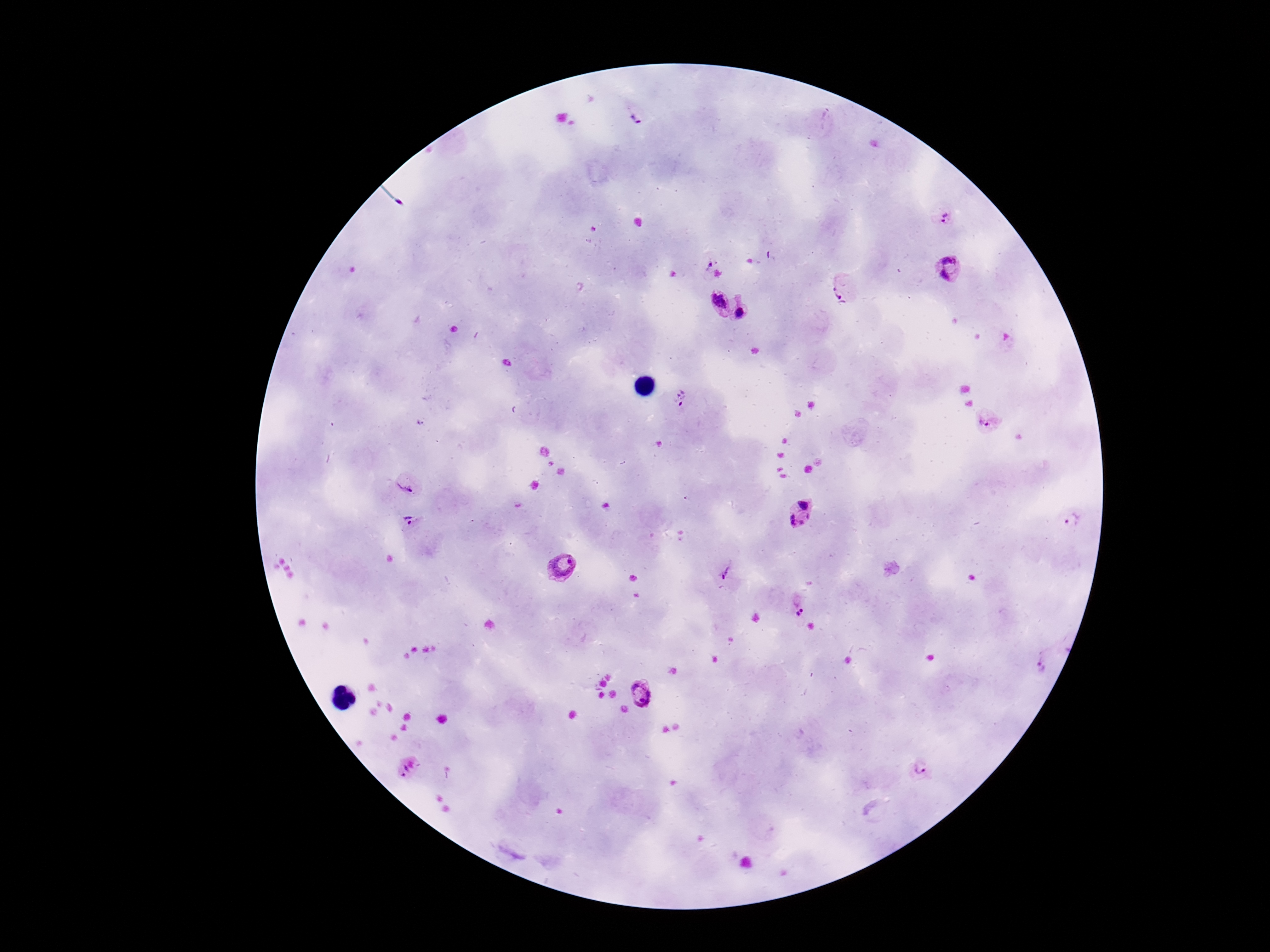

image_size: 1270×952 pixels
stain: Giemsa
magnification: 100x
preparation: thick peripheral-blood smear
field_of_view: one from this slide
patient_malaria_status: infected
plasmodium_parasite_locations: 'approximate object centers, in pixels from the top-left corner: (x=641, y=115), (x=944, y=216), (x=709, y=263), (x=949, y=269), (x=844, y=287), (x=717, y=302), (x=743, y=311), (x=681, y=400), (x=987, y=422), (x=406, y=485), (x=803, y=514), (x=1073, y=519), (x=409, y=522), (x=562, y=567), (x=727, y=573), (x=798, y=601), (x=1039, y=666), (x=641, y=694), (x=920, y=768), (x=411, y=771)'
capture: smartphone camera through the microscope eyepiece